Give the preparation type.
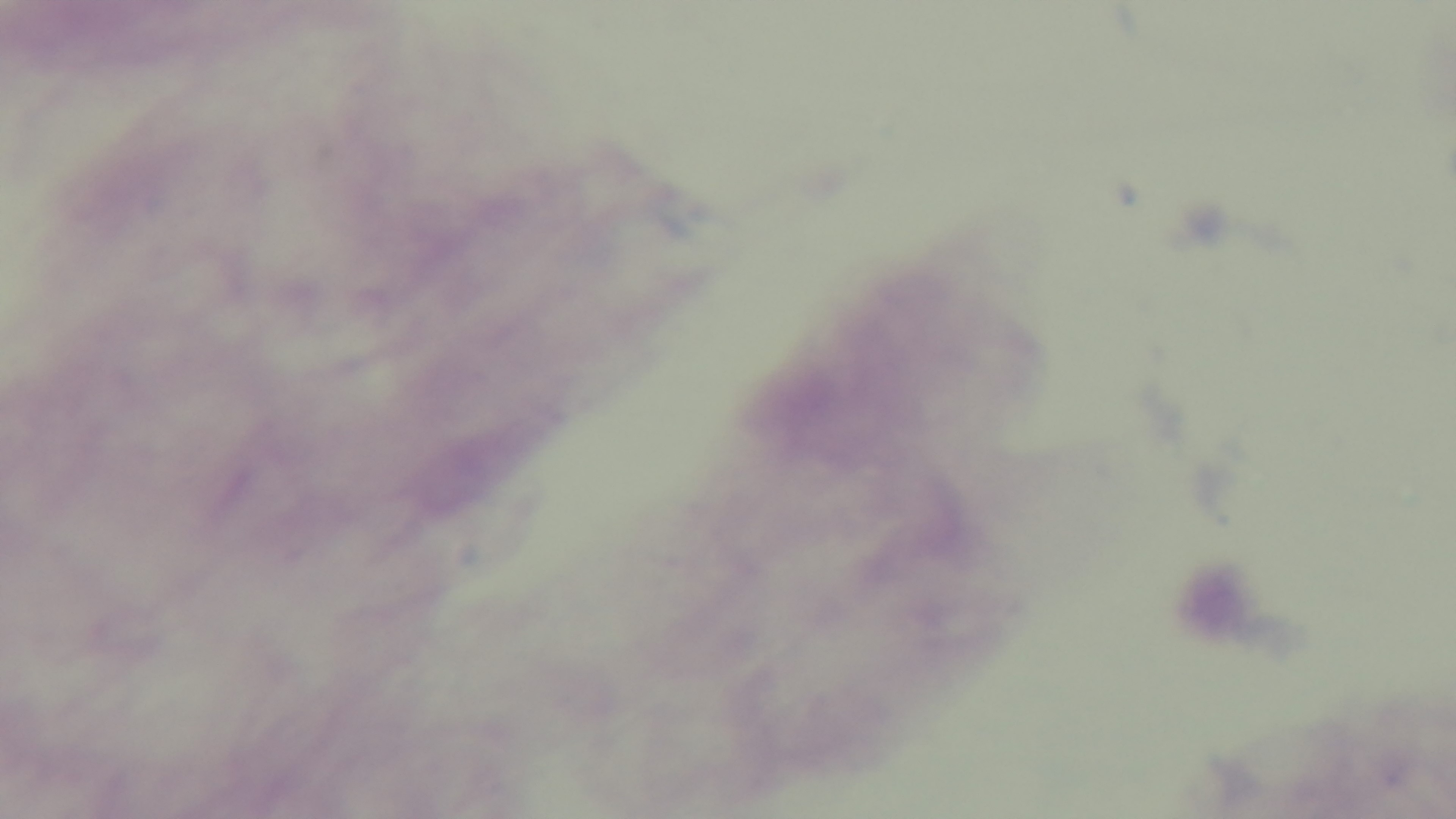

A thick smear.

{
  "malaria_status": "negative",
  "objective": "100x oil immersion",
  "field_of_view": "single",
  "stain": "Giemsa",
  "capture": "mounted 4K digital camera",
  "modality": "light microscopy"
}